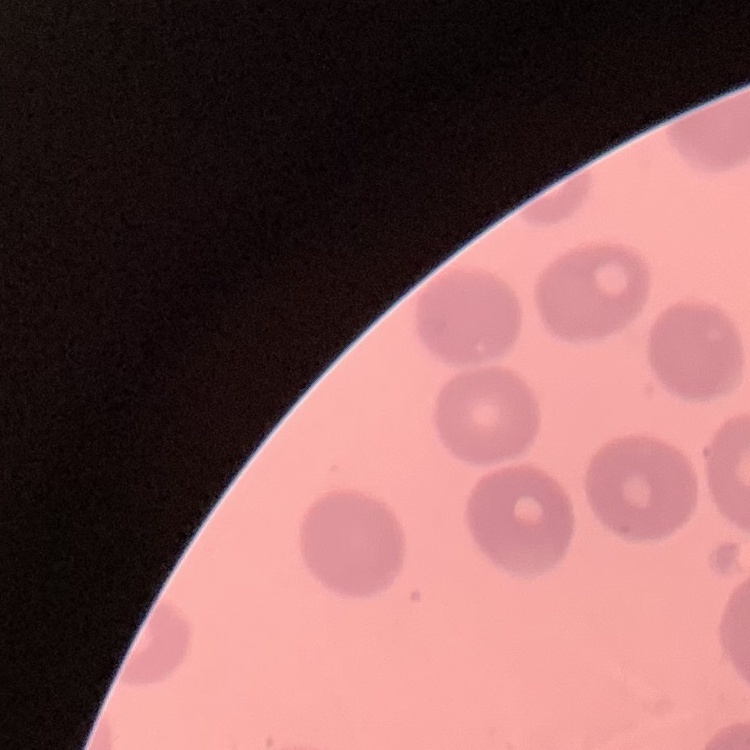 The erythrocytes exhibit no rouleaux formation. Thin blood film. Field's or Giemsa stain. One tile cut from a larger photomicrograph.